Report the malaria status of this cell.
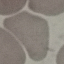
Uninfected.

Summary:
  - Image type: automatically extracted cell patch, resized to 64 × 64 pixels
  - Preparation: thin blood smear
  - Capture: smartphone through the microscope eyepiece
  - Stain: Giemsa